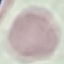
Summary:
  - Result: negative for malaria parasites
  - Capture: smartphone camera at the microscope eyepiece
  - Stain: Giemsa
  - Preparation: thin smear
  - Image type: automatically extracted cell patch, resized to 64 × 64 pixels